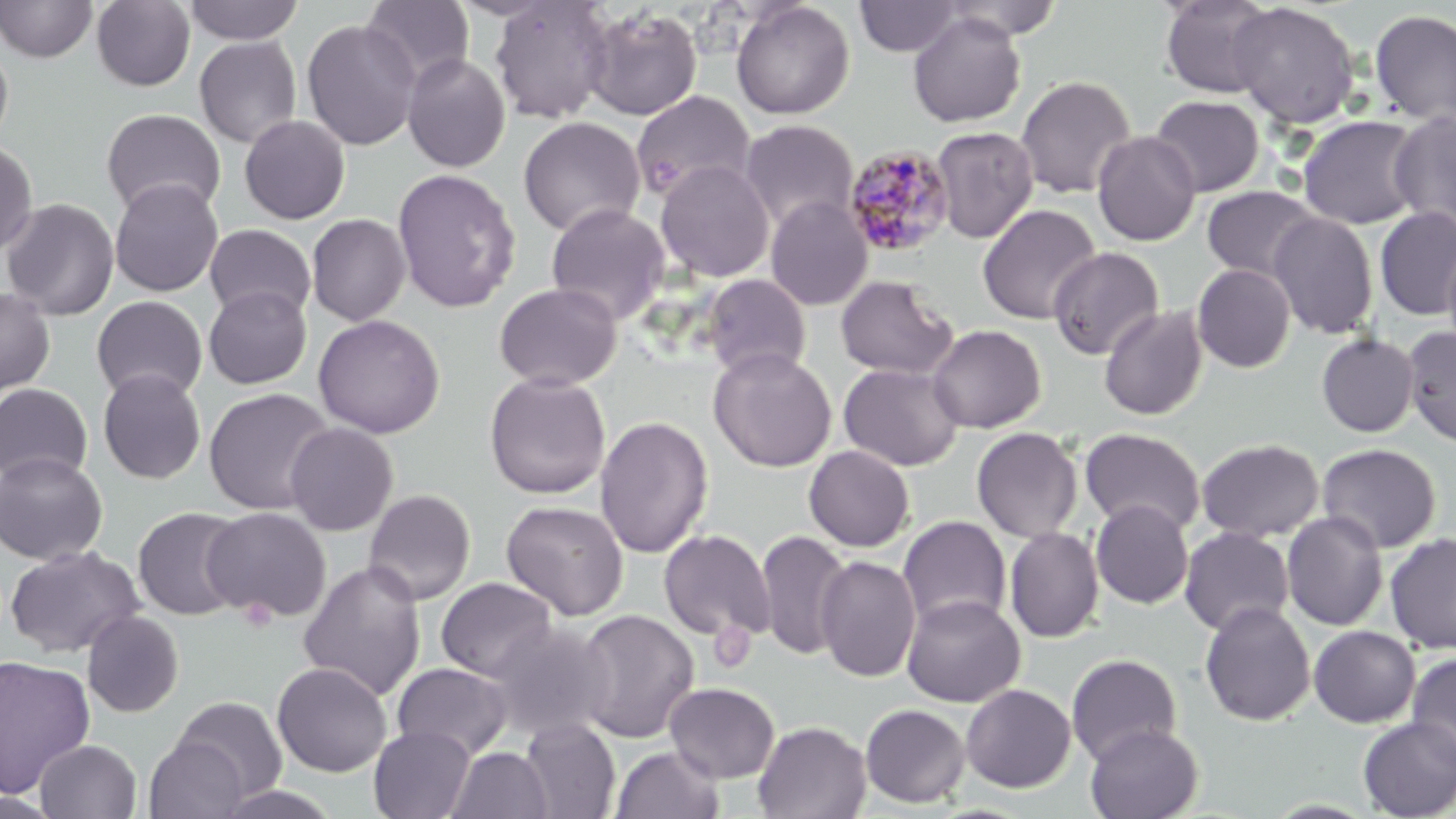
Approximate bounding boxes as (x1,y1)-(x2,y2) corner pairs in pixels. Plasmodium malariae-infected red blood cell locations: (842,143)-(955,258). Platelet locations: (238,597)-(277,632). Uninfected red blood cell locations: (0,0)-(98,62), (183,0)-(305,45), (854,0)-(965,57), (939,0)-(1065,41), (1159,0)-(1278,98), (91,1)-(195,91), (361,1)-(475,89), (489,1)-(614,124), (731,1)-(855,119), (1229,2)-(1360,129), (583,6)-(703,121), (1368,8)-(1456,127), (907,12)-(1026,127), (301,18)-(421,151), (194,36)-(302,148), (0,38)-(14,149), (402,53)-(511,173), (1015,75)-(1137,198), (631,90)-(756,202), (1149,95)-(1265,196), (101,108)-(226,219), (1389,110)-(1456,235), (239,115)-(350,224), (1297,115)-(1424,230), (518,116)-(645,238), (739,119)-(859,234), (930,126)-(1039,244), (1092,130)-(1201,246), (0,139)-(38,258), (656,160)-(775,283), (391,168)-(521,313), (109,179)-(224,297), (1201,185)-(1321,283), (765,196)-(873,311), (1,198)-(120,321), (545,203)-(671,325), (977,204)-(1101,325), (1375,206)-(1456,320), (1268,211)-(1379,339), (306,213)-(411,325), (204,224)-(316,321), (1442,243)-(1456,360), (1048,246)-(1164,360), (1192,264)-(1296,373), (700,274)-(812,381), (835,275)-(958,379), (493,282)-(623,391), (203,285)-(312,389), (0,286)-(56,397), (91,295)-(208,402), (1098,304)-(1208,421), (312,314)-(446,438), (927,324)-(1046,433), (1402,326)-(1456,447), (1316,333)-(1420,437), (708,348)-(837,472), (839,362)-(965,472), (97,368)-(206,484), (484,371)-(611,499), (0,383)-(94,485), (204,387)-(334,515), (595,414)-(713,559), (284,422)-(399,536), (971,426)-(1083,543), (1079,428)-(1207,536), (1196,437)-(1324,543), (1317,442)-(1442,554), (803,445)-(915,551), (0,452)-(108,565), (363,489)-(476,606), (1091,499)-(1194,609), (501,500)-(629,621), (133,506)-(248,621), (202,507)-(332,623), (1282,511)-(1388,632), (898,516)-(1012,634), (1004,527)-(1104,643), (1179,527)-(1295,637), (658,529)-(775,644), (755,529)-(852,661), (1385,532)-(1456,654), (4,545)-(144,658), (815,554)-(921,683), (298,560)-(426,702), (435,577)-(559,684), (901,594)-(1026,707), (1199,601)-(1316,726), (574,608)-(700,743), (82,611)-(184,717), (487,621)-(616,743), (1308,625)-(1420,728), (1066,653)-(1182,766), (1406,653)-(1456,772), (0,655)-(96,798), (272,662)-(392,777), (391,662)-(514,762), (664,682)-(780,783), (960,684)-(1076,793), (171,696)-(288,803), (860,704)-(971,808), (1357,717)-(1456,818), (520,718)-(621,818), (753,720)-(871,819), (1084,723)-(1203,819), (368,725)-(475,819), (144,736)-(248,819), (34,739)-(142,819), (610,744)-(724,819), (446,747)-(552,819), (212,784)-(345,819), (0,792)-(64,818). Slide-level diagnosis: Plasmodium malariae. Light microscopy. One field of a larger specimen. Captured at 1000x magnification. Image is 1456×819 pixels. May-Grünwald-Giemsa-stained preparation. Thin blood film.